Classify this cell by malaria status.
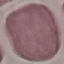
It is uninfected.

Summary:
  - Stain: Giemsa
  - Preparation: thin blood smear
  - Image type: cell patch, automatically extracted from a larger field of view and resized to 64 × 64 pixels
  - Capture: smartphone camera at the microscope eyepiece